Classify this cell by malaria status.
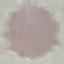

It is uninfected.

capture = smartphone through the microscope eyepiece
preparation = thin blood smear
stain = Giemsa
image type = automatically extracted cell patch, resized to 64 × 64 pixels